Classify this cell by malaria status.
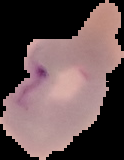
It is parasitized.

From a thin blood film. Image is 124×160 pixels. The area outside the segmented cell region is set to black.